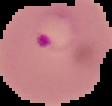

Summary:
  - Result: malaria parasites detected
  - Image size: 112×106 pixels
  - Preparation: thin blood film
  - Image type: cell region segmented out of the field of view; surrounding area masked to black